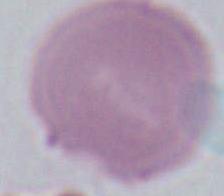

{
  "magnification": "1000x",
  "modality": "micrograph",
  "identification": "erythrocyte"
}